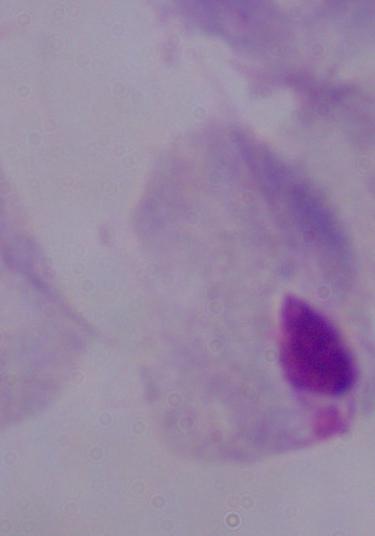
1000x magnification. Photomicrograph. A trichomonad is shown.